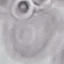

Summary:
  - Malaria status: uninfected
  - Capture: smartphone through the microscope eyepiece
  - Image type: cell patch, automatically extracted from a larger field of view and resized to 64 × 64 pixels
  - Stain: Giemsa
  - Preparation: thin smear